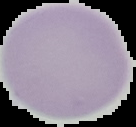

Cell region segmented out of the field of view; the surrounding area is masked to black. Result: no malaria parasites seen. Image is 136×127 pixels. From a thin blood film.